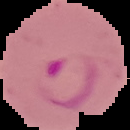

Summary:
  - Image type: segmented cell region with the area outside set to black
  - Image size: 130×130 pixels
  - Preparation: thin blood film
  - Malaria status: parasitized